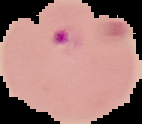

From a thin blood smear. Segmented cell region on a black background. Image is 142×124 pixels. Malaria status: parasitized.